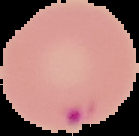

malaria status = parasitized
image size = 139×136 pixels
preparation = thin blood film
image type = cell region segmented out of the field of view; surrounding area masked to black